Report the malaria status of this cell.
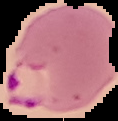

It is parasitized.

image_size: 118×121 pixels
image_type: cell region segmented out of the field of view; surrounding area masked to black
preparation: thin blood film